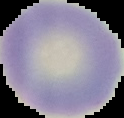
Summary:
  - Image size: 124×118 pixels
  - Malaria status: uninfected
  - Image type: cell region segmented out of the field of view; surrounding area masked to black
  - Preparation: thin blood film